Assess this cell for malaria.
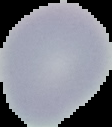
It is uninfected.

Summary:
  - Image type: cell region segmented out of the field of view; surrounding area masked to black
  - Image size: 112×127 pixels
  - Preparation: thin blood film